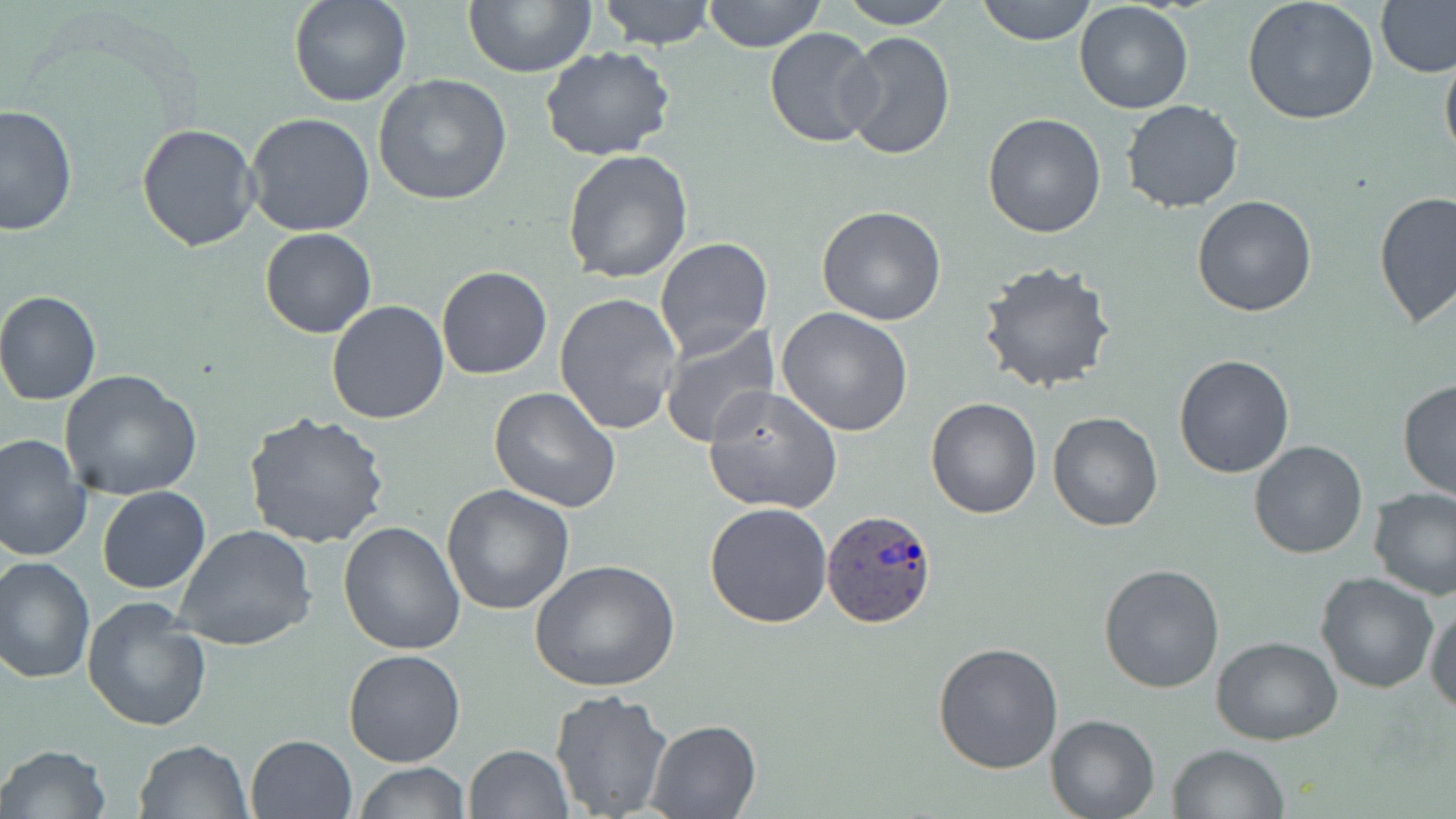

slide-level diagnosis = Plasmodium ovale
modality = optical microscopy
uninfected red blood cell locations = approximate bounding boxes as (x1, y1, x2, y2) in pixels: (288, 0, 414, 108), (465, 0, 596, 76), (597, 0, 717, 48), (702, 0, 826, 52), (836, 0, 959, 28), (976, 0, 1095, 45), (1241, 0, 1380, 125), (1377, 0, 1455, 78), (1073, 2, 1195, 114), (764, 27, 883, 148), (840, 31, 956, 161), (1440, 42, 1456, 166), (538, 46, 678, 163), (374, 75, 514, 207), (1121, 100, 1244, 213), (1, 104, 77, 236), (244, 112, 375, 238), (983, 113, 1108, 238), (135, 123, 260, 252), (563, 149, 695, 284), (1374, 191, 1455, 328), (1192, 195, 1319, 317), (816, 206, 947, 327), (260, 228, 378, 339), (655, 237, 772, 360), (975, 259, 1119, 394), (436, 266, 553, 381), (0, 290, 102, 405), (554, 293, 684, 435), (326, 300, 451, 424), (776, 306, 915, 436), (658, 325, 778, 448), (1172, 353, 1295, 478), (60, 370, 204, 500), (1397, 379, 1455, 501), (703, 386, 843, 515), (489, 387, 622, 515), (926, 397, 1041, 518), (242, 411, 391, 551), (1048, 412, 1163, 532), (0, 433, 93, 564), (1248, 439, 1368, 559), (441, 484, 575, 615), (1368, 486, 1456, 599), (96, 487, 211, 594), (704, 501, 834, 629), (338, 520, 468, 655), (174, 524, 316, 652), (0, 556, 96, 685), (529, 559, 679, 692), (1097, 563, 1225, 693), (1315, 572, 1440, 695), (81, 598, 210, 731), (1425, 602, 1456, 713), (1213, 637, 1341, 745), (932, 641, 1064, 775), (342, 647, 467, 768), (548, 687, 674, 817), (1046, 712, 1160, 818), (644, 718, 763, 818), (246, 734, 358, 819), (133, 738, 253, 819), (1168, 743, 1289, 818), (0, 744, 112, 819), (462, 744, 574, 819), (353, 761, 471, 818)
stain = May-Grünwald-Giemsa
preparation = thin blood film
magnification = 1000x
field of view = one of a larger specimen
Plasmodium ovale-infected red blood cell locations = approximate bounding boxes as (x1, y1, x2, y2) in pixels: (821, 508, 938, 630)
image size = 1456×819 pixels